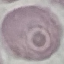

result = negative for malaria parasites
capture = smartphone through the microscope eyepiece
stain = Giemsa
preparation = thin blood film
image type = cell patch, automatically extracted from a larger field of view and resized to 64 × 64 pixels